Assess this cell for malaria.
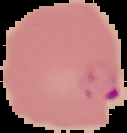
Parasitized.

image size = 127×133 pixels
image type = segmented cell region on a black background
preparation = thin blood smear